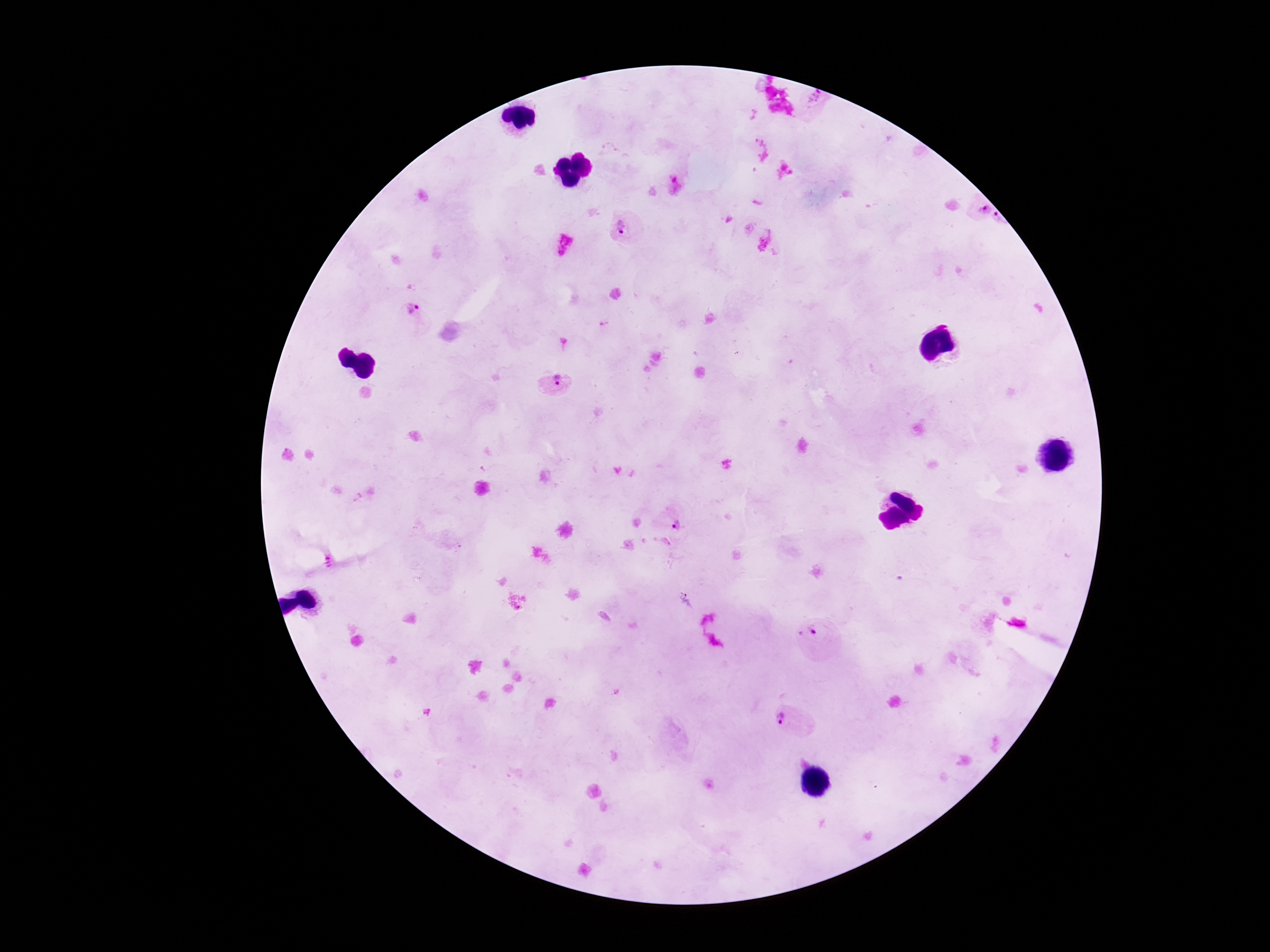

Approximate object centers, in pixels from the top-left corner.
Summary:
  - Plasmodium parasite locations: (x=675, y=183), (x=979, y=209), (x=998, y=219), (x=624, y=227), (x=411, y=314), (x=555, y=383), (x=672, y=521), (x=813, y=637), (x=790, y=721)
  - Field of view: one from this slide
  - Stain: Giemsa
  - Preparation: thick blood smear
  - Magnification: 100x
  - Patient malaria status: positive
  - Capture: smartphone camera through the microscope eyepiece
  - Image size: 1270×952 pixels